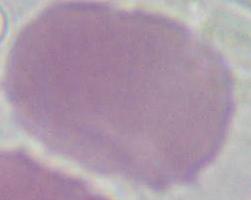
{
  "modality": "photomicrograph",
  "magnification": "1000x",
  "identification": "erythrocyte"
}